Point out each Plasmodium parasite and each leukocyte.
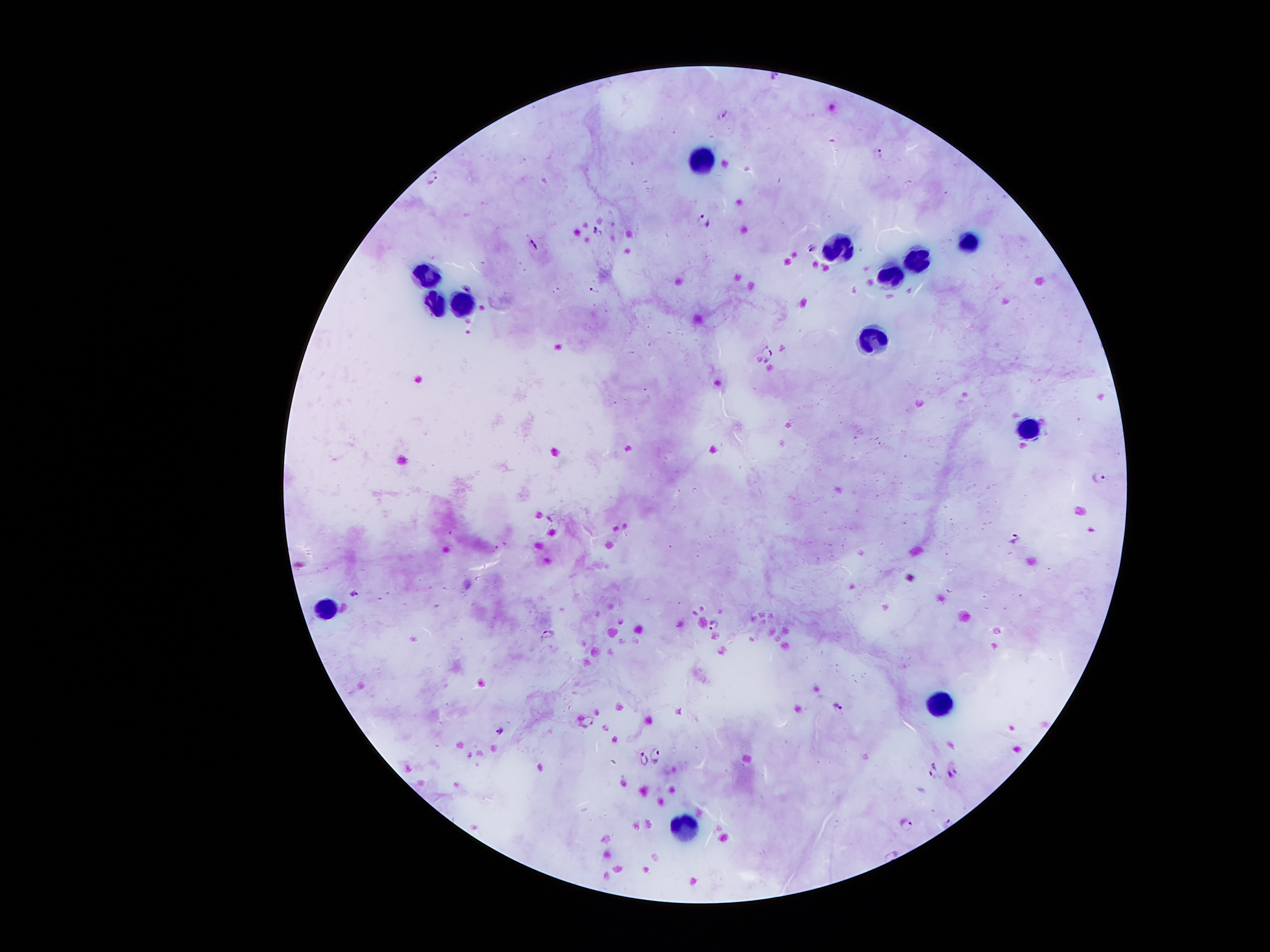

Approximate centers as (x, y) in pixels.
Plasmodium parasites: (776, 73), (724, 113), (879, 151), (433, 177), (704, 220), (596, 231), (532, 242), (812, 247), (467, 287), (768, 350), (1099, 478), (551, 516), (1014, 536), (355, 590), (713, 623), (548, 635), (838, 707), (589, 720), (499, 729), (656, 753), (639, 756), (952, 771), (932, 772), (947, 821), (904, 822).
Leukocytes: (697, 163), (965, 242), (839, 247), (916, 260), (890, 273), (423, 276), (432, 305), (460, 305), (872, 335), (1033, 429), (323, 604), (938, 704), (685, 827).

Summary:
  - Magnification: 100x
  - Patient malaria status: positive for Plasmodium falciparum
  - Capture: smartphone camera through the microscope eyepiece
  - Field of view: single
  - Image size: 1270×952 pixels
  - Preparation: thick blood film
  - Stain: Giemsa